Classify this cell by malaria status.
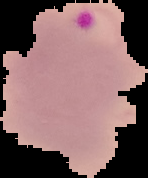

It is parasitized.

Summary:
  - Image size: 148×178 pixels
  - Image type: cell region segmented out of the field of view; surrounding area masked to black
  - Preparation: thin blood film